Locate cells.
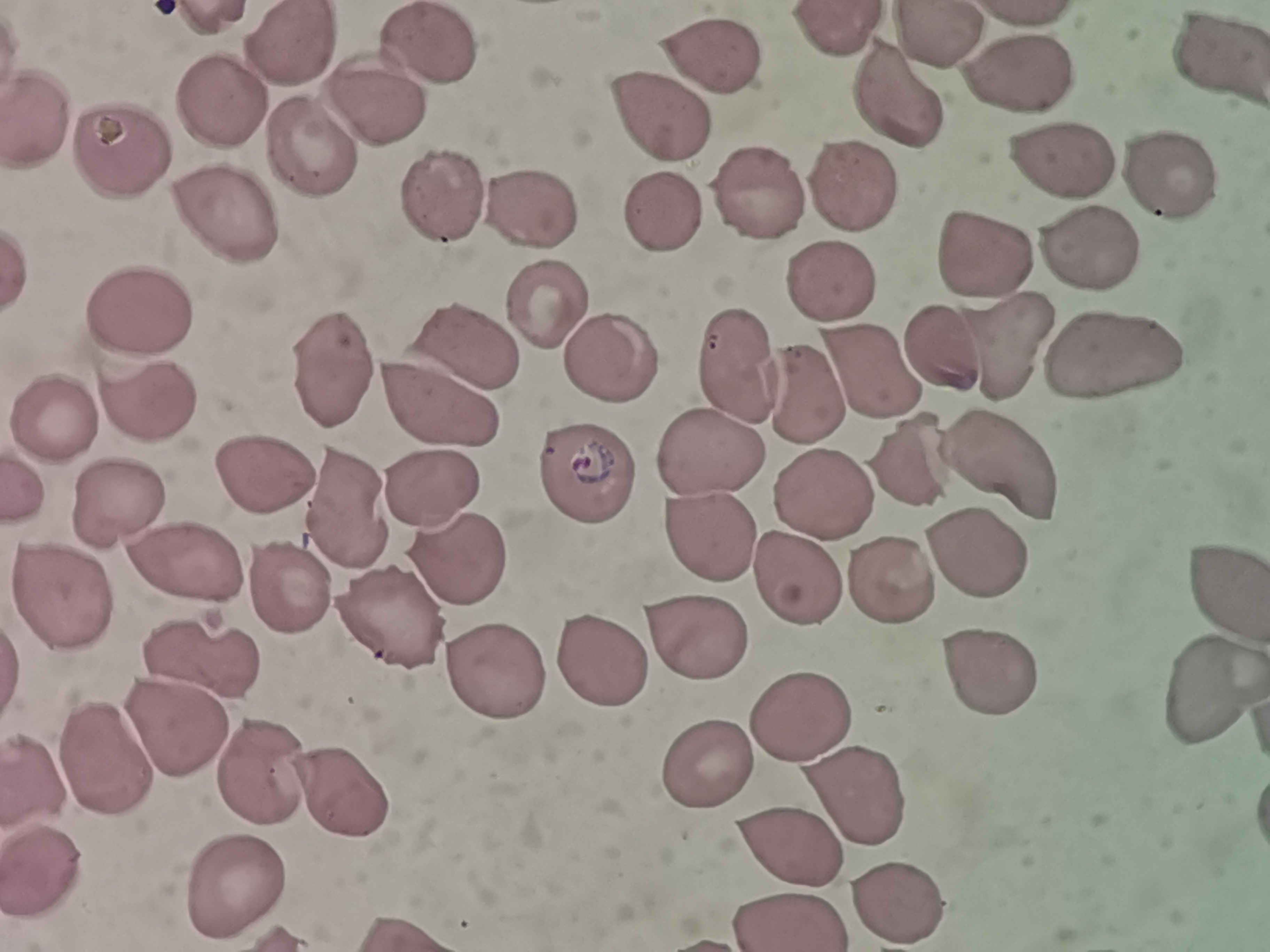

Approximate centers as [x, y] in pixels.
Cells: [837, 31], [934, 39], [430, 43], [295, 44], [708, 58], [1222, 62], [1011, 68], [379, 90], [218, 99], [895, 105], [661, 110], [45, 119], [122, 139], [313, 146], [1062, 163], [1164, 172], [845, 188], [760, 201], [222, 204], [442, 204], [534, 207], [665, 219], [984, 247], [1084, 253], [828, 284], [542, 302], [138, 311], [946, 344], [466, 345], [998, 350], [605, 353], [1106, 356], [738, 362], [333, 363], [869, 373], [804, 392], [150, 396], [440, 403], [51, 411], [715, 448], [916, 460], [1007, 463], [258, 473], [583, 473], [431, 484], [826, 494], [125, 502], [703, 534], [459, 556], [972, 556], [192, 569], [800, 574], [890, 583], [1221, 583], [63, 589], [289, 596], [384, 615], [691, 634], [600, 658], [204, 660], [492, 672], [984, 674], [1207, 690], [805, 704], [179, 733], [700, 751], [111, 756], [266, 767], [345, 791], [848, 793], [780, 841], [47, 872], [241, 881], [902, 896], [790, 918].

{
  "stain": "Giemsa",
  "preparation": "thin blood film",
  "capture": "smartphone through the microscope eyepiece",
  "field_of_view": "single",
  "image_size": "1270×952 pixels"
}